Name the parasite shown.
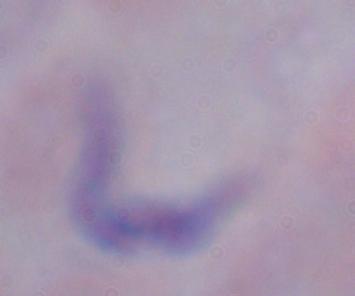

This is a trypanosome.

{
  "modality": "micrograph",
  "magnification": "1000x"
}